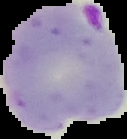
Result: malaria parasites detected. The area outside the segmented cell region is set to black. From a thin blood film. Image is 127×139 pixels.